Report the malaria status of this cell.
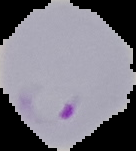
It is parasitized.

The area outside the segmented cell region is set to black. Image is 136×151 pixels. From a thin blood smear.